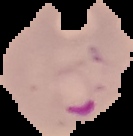
From a thin blood film. Segmented cell region on a black background. Malaria status: parasitized. Image is 133×136 pixels.